Classify this cell by malaria status.
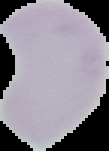

Uninfected.

Image is 109×151 pixels. Segmented cell region on a black background. From a thin blood film.